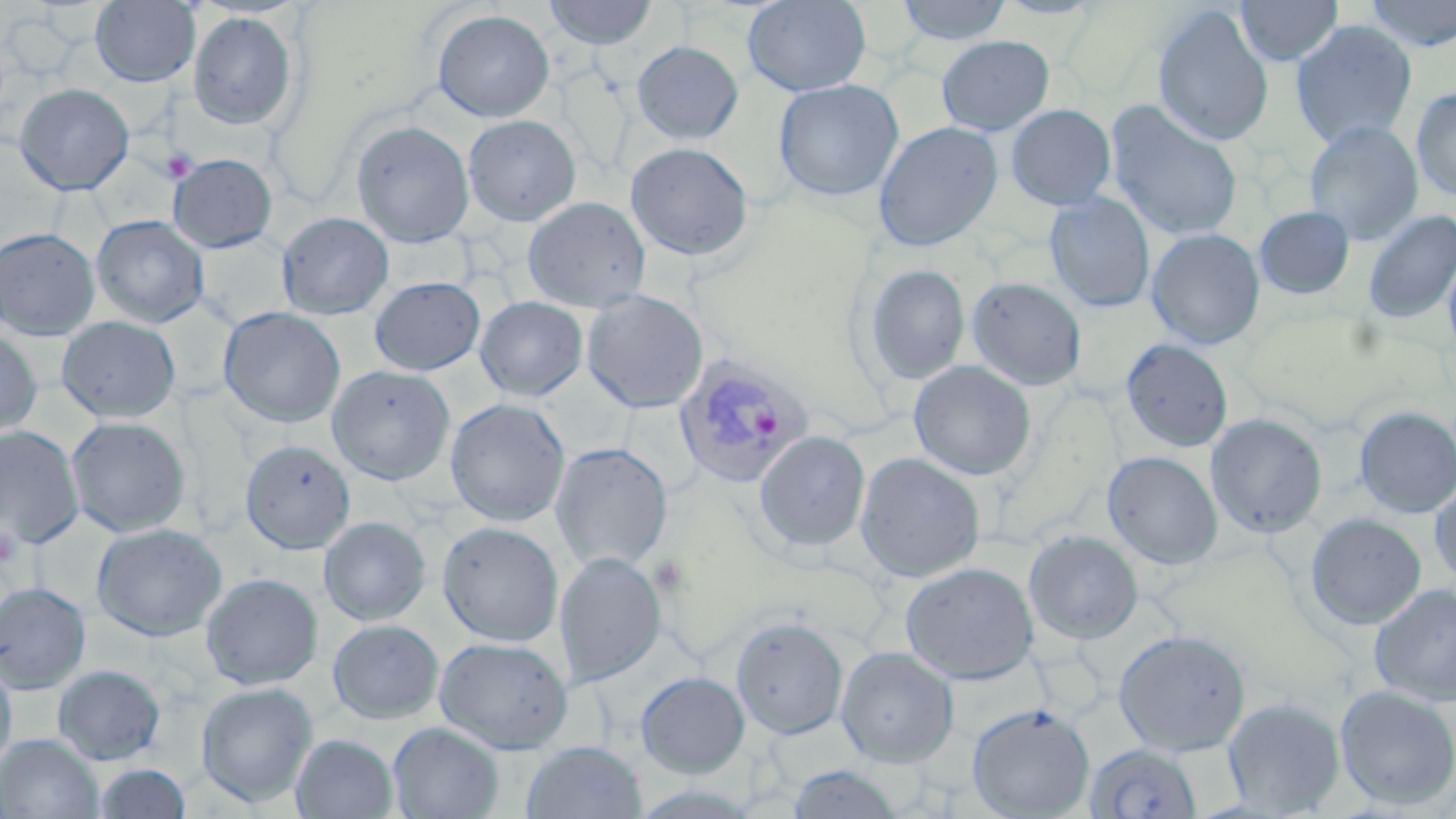
Summary:
  - Coordinate format: approximate bounding boxes as named x1/y1/x2/y2 corners in pixels
  - Plasmodium vivax-infected red blood cell locations: (x1=674, y1=355, x2=813, y2=489)
  - Platelet locations: (x1=162, y1=149, x2=198, y2=182), (x1=0, y1=526, x2=19, y2=566)
  - Uninfected red blood cell locations: (x1=90, y1=0, x2=200, y2=87), (x1=543, y1=0, x2=658, y2=49), (x1=743, y1=0, x2=871, y2=96), (x1=895, y1=0, x2=1011, y2=45), (x1=992, y1=0, x2=1108, y2=19), (x1=1233, y1=0, x2=1344, y2=66), (x1=1360, y1=0, x2=1456, y2=52), (x1=1152, y1=5, x2=1274, y2=147), (x1=433, y1=9, x2=555, y2=122), (x1=187, y1=11, x2=298, y2=130), (x1=1290, y1=20, x2=1417, y2=150), (x1=937, y1=35, x2=1054, y2=135), (x1=631, y1=41, x2=743, y2=144), (x1=773, y1=79, x2=903, y2=201), (x1=14, y1=82, x2=134, y2=195), (x1=1411, y1=86, x2=1456, y2=200), (x1=1106, y1=101, x2=1244, y2=241), (x1=1006, y1=104, x2=1115, y2=210), (x1=463, y1=115, x2=581, y2=226), (x1=352, y1=120, x2=473, y2=247), (x1=873, y1=121, x2=1003, y2=252), (x1=1304, y1=121, x2=1423, y2=244), (x1=626, y1=143, x2=753, y2=262), (x1=168, y1=153, x2=278, y2=253), (x1=1044, y1=192, x2=1155, y2=312), (x1=522, y1=197, x2=651, y2=312), (x1=1254, y1=205, x2=1355, y2=300), (x1=1362, y1=210, x2=1456, y2=325), (x1=277, y1=212, x2=394, y2=319), (x1=92, y1=215, x2=209, y2=328), (x1=0, y1=227, x2=99, y2=340), (x1=1146, y1=229, x2=1265, y2=350), (x1=1442, y1=248, x2=1456, y2=360), (x1=862, y1=263, x2=970, y2=385), (x1=370, y1=277, x2=485, y2=375), (x1=966, y1=277, x2=1087, y2=390), (x1=581, y1=291, x2=708, y2=413), (x1=475, y1=296, x2=588, y2=401), (x1=218, y1=306, x2=346, y2=428), (x1=56, y1=316, x2=180, y2=423), (x1=0, y1=328, x2=42, y2=438), (x1=1121, y1=338, x2=1233, y2=452), (x1=909, y1=360, x2=1036, y2=480), (x1=328, y1=365, x2=454, y2=485), (x1=445, y1=398, x2=569, y2=526), (x1=1354, y1=406, x2=1456, y2=518), (x1=1205, y1=413, x2=1327, y2=539), (x1=66, y1=416, x2=191, y2=537), (x1=0, y1=426, x2=84, y2=549), (x1=754, y1=430, x2=870, y2=552), (x1=240, y1=440, x2=355, y2=554), (x1=551, y1=442, x2=672, y2=571), (x1=1102, y1=451, x2=1223, y2=570), (x1=855, y1=452, x2=985, y2=582), (x1=1429, y1=478, x2=1456, y2=589), (x1=1304, y1=512, x2=1426, y2=630), (x1=319, y1=517, x2=431, y2=625), (x1=437, y1=521, x2=563, y2=647), (x1=91, y1=523, x2=227, y2=642), (x1=1023, y1=529, x2=1143, y2=644), (x1=555, y1=551, x2=666, y2=686), (x1=900, y1=562, x2=1038, y2=684), (x1=201, y1=573, x2=323, y2=690), (x1=0, y1=583, x2=91, y2=694), (x1=1369, y1=583, x2=1456, y2=706), (x1=731, y1=616, x2=848, y2=739), (x1=328, y1=619, x2=444, y2=724), (x1=1113, y1=630, x2=1251, y2=755), (x1=434, y1=637, x2=572, y2=754), (x1=836, y1=646, x2=959, y2=767), (x1=0, y1=656, x2=16, y2=775), (x1=53, y1=664, x2=166, y2=765), (x1=636, y1=672, x2=749, y2=777), (x1=196, y1=681, x2=318, y2=807), (x1=1334, y1=685, x2=1456, y2=810), (x1=1221, y1=697, x2=1346, y2=817), (x1=966, y1=703, x2=1095, y2=818), (x1=388, y1=722, x2=504, y2=819), (x1=0, y1=734, x2=103, y2=818), (x1=291, y1=734, x2=398, y2=818), (x1=521, y1=741, x2=647, y2=818), (x1=1085, y1=742, x2=1204, y2=818), (x1=93, y1=763, x2=192, y2=819), (x1=787, y1=763, x2=905, y2=819)
  - Slide-level diagnosis: Plasmodium vivax
  - Stain: May-Grünwald-Giemsa
  - Modality: optical microscopy
  - Magnification: 1000x
  - Image size: 1456×819 pixels
  - Field of view: one of a larger specimen
  - Preparation: thin blood smear